Locate every Plasmodium ovale-infected red blood cell.
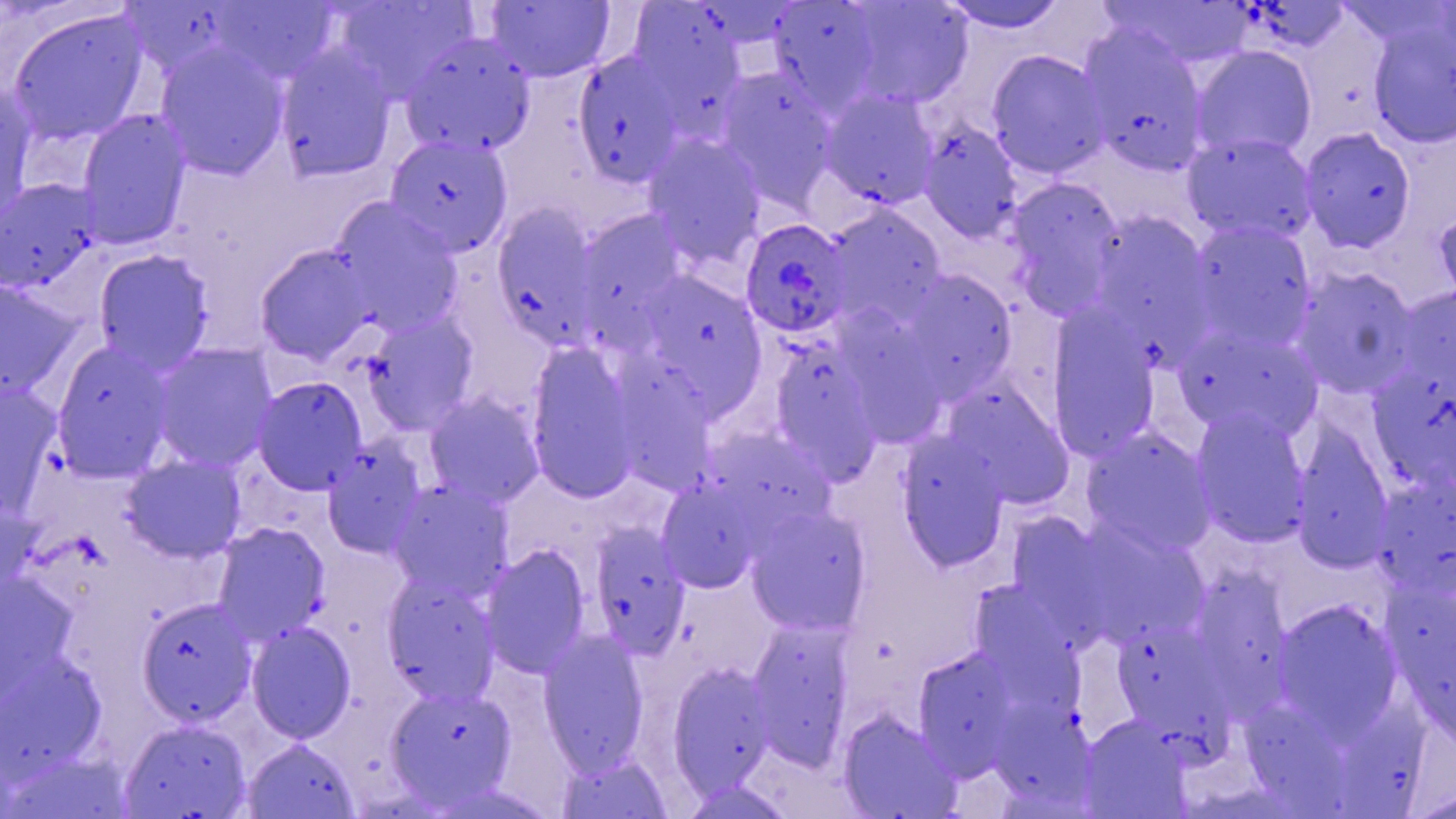
Approximate bounding boxes as (x1,y1)-(x2,y2) corner pairs in pixels.
Plasmodium ovale-infected red blood cells: (740,218)-(852,338).

slide-level diagnosis = Plasmodium ovale
field of view = one of a larger specimen
magnification = 1000x
uninfected red blood cell locations = approximate bounding boxes as (x1,y1)-(x2,y2) corner pairs in pixels: (331,0)-(477,103), (837,0)-(975,111), (119,1)-(242,80), (210,1)-(340,84), (485,1)-(617,83), (626,1)-(748,120), (767,1)-(886,117), (936,1)-(1070,34), (1101,1)-(1254,69), (7,8)-(150,146), (1367,18)-(1456,148), (1078,24)-(1211,176), (400,31)-(537,158), (155,42)-(290,181), (275,42)-(397,182), (1192,46)-(1316,161), (572,50)-(688,186), (986,50)-(1110,178), (714,67)-(840,213), (0,82)-(38,227), (819,89)-(940,209), (76,109)-(191,250), (917,121)-(1024,241), (1300,128)-(1415,253), (642,133)-(765,268), (1183,133)-(1317,244), (384,134)-(513,257), (1005,177)-(1124,316), (1,179)-(102,294), (332,198)-(464,334), (491,201)-(603,349), (825,203)-(948,326), (1433,206)-(1456,312), (576,208)-(691,328), (1089,212)-(1214,340), (1188,220)-(1317,351), (255,245)-(375,366), (93,249)-(214,373), (1293,267)-(1418,399), (897,269)-(1018,399), (638,271)-(763,389), (0,278)-(81,400), (1394,287)-(1456,397), (1046,308)-(1161,460), (363,311)-(480,435), (1173,325)-(1321,441), (770,336)-(879,472), (524,341)-(641,504), (52,342)-(174,480), (151,343)-(277,473), (615,350)-(723,499), (1372,372)-(1456,489), (253,377)-(367,495), (945,380)-(1072,508), (0,382)-(63,514), (425,393)-(545,507), (1190,409)-(1311,548), (1292,427)-(1394,572), (1081,428)-(1217,558), (896,434)-(1010,572), (323,440)-(427,558), (706,447)-(843,528), (122,455)-(245,563), (656,476)-(764,594), (388,480)-(513,598), (1373,480)-(1456,599), (0,495)-(42,598), (745,504)-(871,634), (1005,512)-(1114,629), (1070,521)-(1210,647), (212,523)-(330,644), (589,524)-(690,657), (480,544)-(591,678), (1205,557)-(1300,721), (0,571)-(77,709), (381,572)-(499,705), (969,583)-(1076,695), (136,598)-(256,725), (1273,599)-(1403,739), (1111,618)-(1232,747), (746,620)-(854,770), (246,621)-(357,743), (537,631)-(650,775), (912,647)-(1027,777), (0,651)-(108,782), (667,661)-(775,792), (386,684)-(517,806), (992,692)-(1101,798), (1237,704)-(1359,819), (836,710)-(961,819), (1079,715)-(1190,818), (118,718)-(252,819), (241,737)-(361,819), (555,752)-(674,819), (678,778)-(799,818), (1407,785)-(1455,818)
stain = May-Grünwald-Giemsa
preparation = thin blood film
image size = 1456×819 pixels
modality = light microscopy